Outline each blood parasite and name the species.
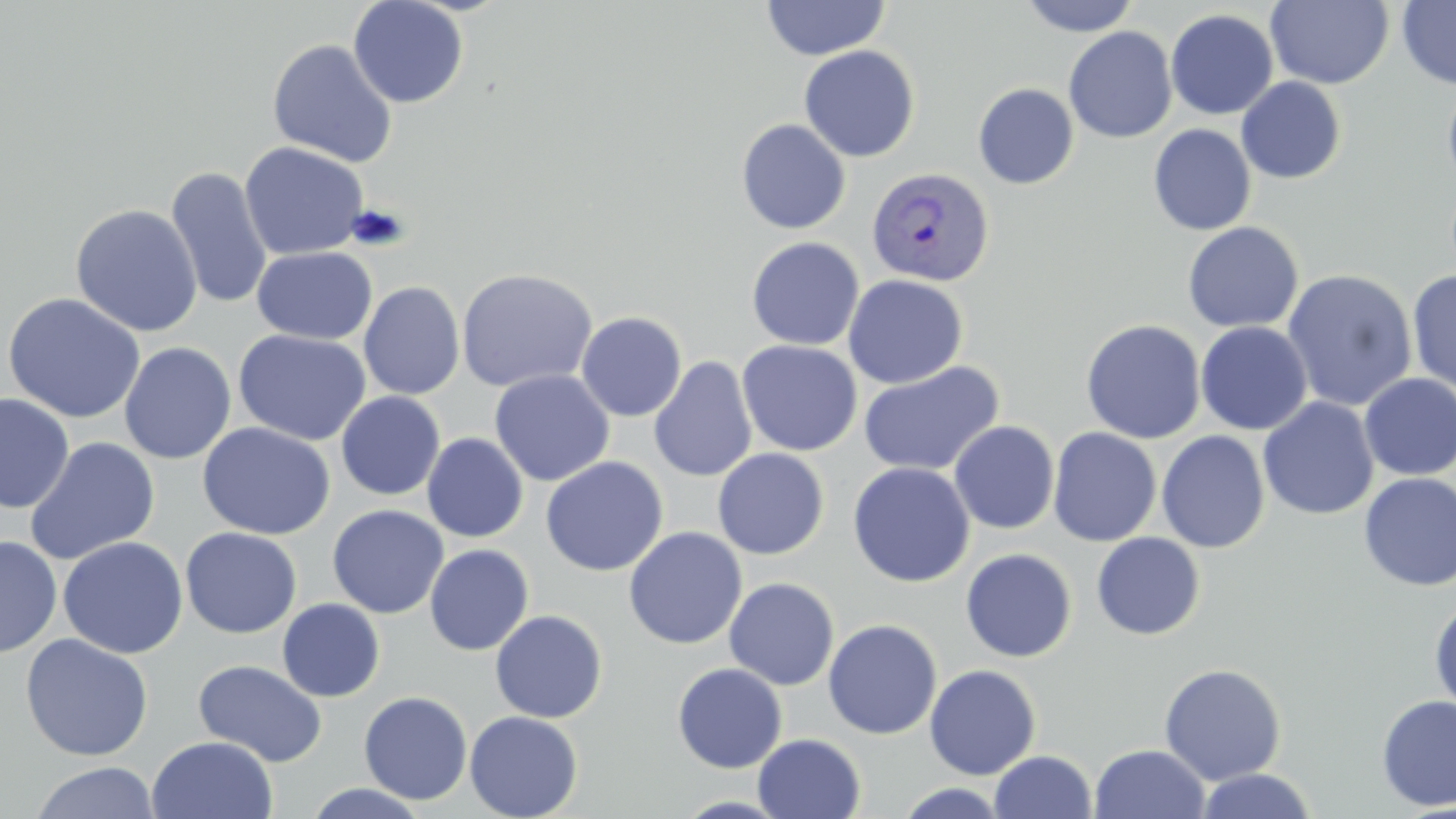

Approximate bounding boxes as [x1, y1, x2, y2] in pixels.
Plasmodium vivax-infected red blood cells: [866, 165, 995, 286].
No Plasmodium falciparum, Plasmodium ovale, Plasmodium malariae, Babesia divergens, or Trypanosoma brucei observed.

Summary:
  - Uninfected red blood cell locations: [348, 0, 470, 108], [762, 0, 889, 61], [1018, 0, 1141, 36], [1266, 0, 1394, 89], [1397, 0, 1456, 90], [1165, 8, 1279, 120], [1063, 26, 1178, 143], [267, 38, 398, 167], [799, 45, 920, 162], [1236, 77, 1346, 184], [1441, 79, 1456, 194], [973, 83, 1079, 189], [736, 118, 851, 234], [1148, 124, 1256, 235], [239, 141, 370, 261], [166, 166, 273, 310], [70, 203, 203, 338], [1182, 221, 1304, 333], [746, 237, 865, 351], [251, 246, 378, 344], [456, 267, 598, 393], [1281, 269, 1418, 412], [1407, 269, 1456, 397], [843, 274, 968, 389], [358, 281, 466, 399], [2, 292, 146, 424], [575, 311, 687, 422], [1081, 319, 1206, 444], [1195, 321, 1313, 435], [233, 329, 371, 446], [736, 339, 863, 457], [119, 341, 237, 464], [648, 356, 758, 482], [858, 360, 1005, 477], [489, 370, 614, 486], [1359, 374, 1456, 481], [336, 391, 445, 501], [0, 393, 75, 513], [1258, 397, 1379, 520], [949, 420, 1060, 534], [197, 422, 336, 540], [1047, 427, 1162, 547], [1156, 431, 1270, 553], [422, 432, 529, 543], [24, 437, 161, 565], [712, 448, 829, 560], [540, 457, 667, 576], [847, 462, 975, 588], [1358, 473, 1456, 591], [327, 504, 449, 619], [623, 526, 748, 649], [181, 527, 302, 638], [1091, 532, 1206, 640], [0, 535, 61, 658], [58, 536, 189, 659], [424, 544, 534, 656], [960, 548, 1077, 663], [723, 577, 840, 691], [277, 598, 385, 702], [1429, 598, 1456, 715], [490, 609, 608, 723], [823, 619, 942, 739], [19, 633, 154, 761], [193, 659, 327, 767], [671, 662, 788, 773], [1158, 662, 1286, 785], [924, 664, 1041, 779], [359, 691, 473, 805], [1376, 694, 1456, 812], [464, 711, 583, 819], [753, 733, 866, 819], [146, 735, 279, 819], [1089, 744, 1211, 819], [990, 750, 1096, 818], [29, 761, 161, 819], [1195, 768, 1319, 819], [303, 783, 431, 819], [894, 783, 1013, 818]
  - Slide-level diagnosis: Plasmodium vivax
  - Field of view: single
  - Magnification: 1000x
  - Image size: 1456×819 pixels
  - Stain: May-Grünwald-Giemsa
  - Modality: light microscopy
  - Preparation: thin blood film